Outline each Plasmodium vivax-infected red blood cell.
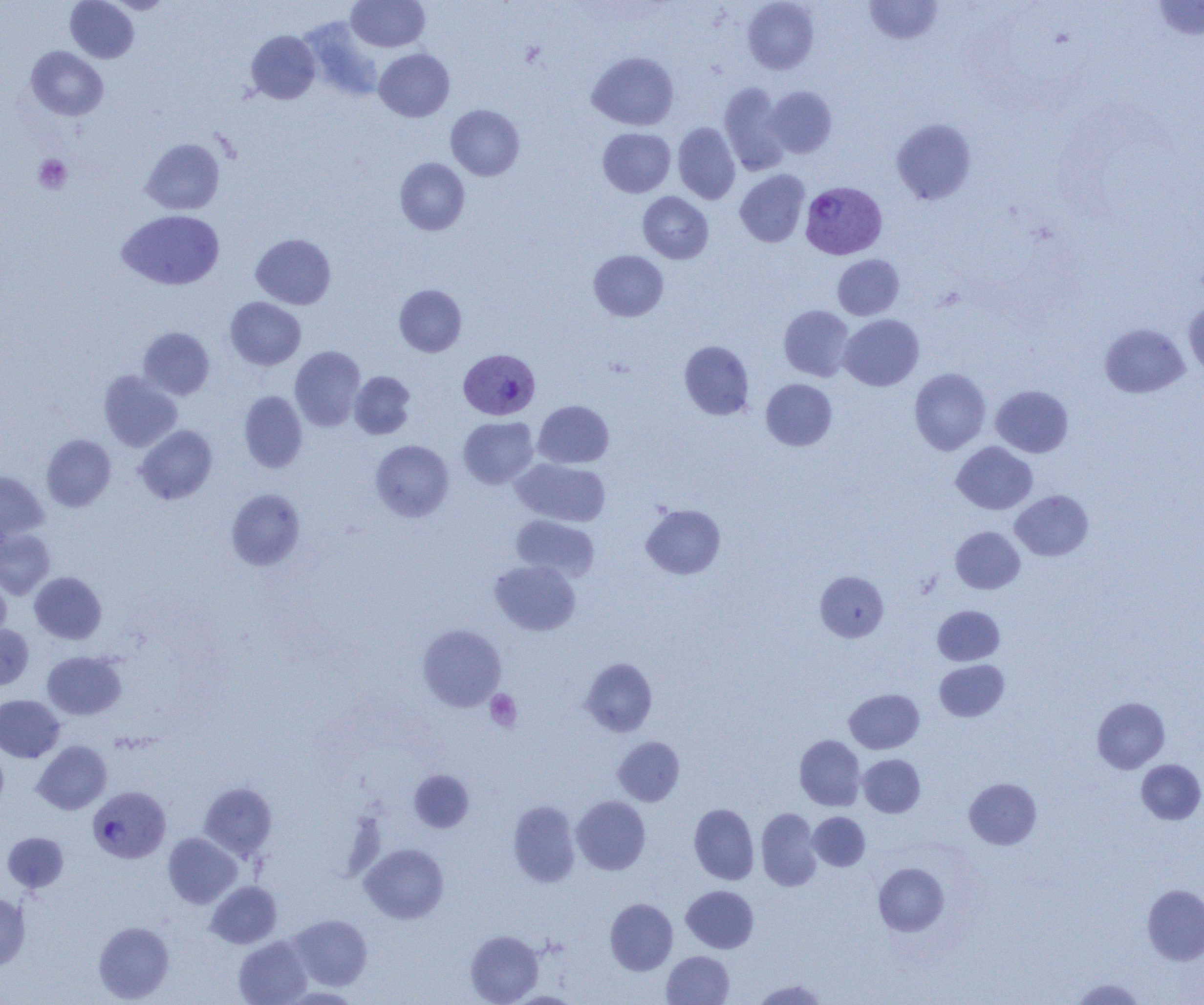
Approximate bounding boxes as named x1/y1/x2/y2 corners in pixels.
Plasmodium vivax-infected red blood cells: (x1=800, y1=181, x2=887, y2=259), (x1=459, y1=348, x2=541, y2=420), (x1=88, y1=786, x2=170, y2=863).

Uninfected red blood cell locations: (x1=65, y1=0, x2=138, y2=63), (x1=106, y1=0, x2=174, y2=14), (x1=347, y1=0, x2=430, y2=52), (x1=864, y1=0, x2=944, y2=45), (x1=1151, y1=0, x2=1204, y2=42), (x1=742, y1=1, x2=819, y2=74), (x1=300, y1=17, x2=383, y2=102), (x1=246, y1=31, x2=320, y2=104), (x1=26, y1=46, x2=108, y2=121), (x1=374, y1=48, x2=454, y2=121), (x1=587, y1=51, x2=679, y2=130), (x1=719, y1=83, x2=790, y2=175), (x1=765, y1=86, x2=837, y2=157), (x1=446, y1=104, x2=525, y2=180), (x1=891, y1=118, x2=976, y2=205), (x1=673, y1=122, x2=741, y2=204), (x1=597, y1=127, x2=675, y2=198), (x1=141, y1=138, x2=225, y2=215), (x1=395, y1=157, x2=469, y2=235), (x1=735, y1=169, x2=810, y2=247), (x1=638, y1=192, x2=713, y2=264), (x1=117, y1=209, x2=224, y2=290), (x1=251, y1=233, x2=336, y2=309), (x1=588, y1=250, x2=668, y2=322), (x1=832, y1=254, x2=904, y2=320), (x1=394, y1=285, x2=466, y2=356), (x1=225, y1=297, x2=306, y2=370), (x1=1184, y1=298, x2=1204, y2=378), (x1=778, y1=305, x2=854, y2=381), (x1=838, y1=314, x2=924, y2=391), (x1=1100, y1=323, x2=1189, y2=398), (x1=138, y1=327, x2=214, y2=399), (x1=679, y1=340, x2=754, y2=420), (x1=290, y1=346, x2=366, y2=430), (x1=909, y1=367, x2=991, y2=455), (x1=99, y1=371, x2=182, y2=452), (x1=349, y1=371, x2=416, y2=439), (x1=761, y1=379, x2=837, y2=451), (x1=991, y1=385, x2=1073, y2=458), (x1=239, y1=391, x2=308, y2=473), (x1=533, y1=400, x2=614, y2=468), (x1=458, y1=416, x2=538, y2=488), (x1=135, y1=425, x2=217, y2=504), (x1=41, y1=434, x2=116, y2=511), (x1=370, y1=440, x2=454, y2=521), (x1=951, y1=441, x2=1037, y2=514), (x1=511, y1=458, x2=610, y2=526), (x1=0, y1=470, x2=48, y2=544), (x1=226, y1=489, x2=305, y2=570), (x1=1010, y1=490, x2=1094, y2=561), (x1=641, y1=504, x2=725, y2=579), (x1=511, y1=515, x2=599, y2=581), (x1=950, y1=526, x2=1025, y2=593), (x1=0, y1=529, x2=55, y2=600), (x1=490, y1=560, x2=580, y2=635), (x1=815, y1=571, x2=888, y2=642), (x1=30, y1=572, x2=107, y2=644), (x1=0, y1=573, x2=11, y2=643), (x1=933, y1=605, x2=1004, y2=665), (x1=0, y1=624, x2=33, y2=690), (x1=417, y1=624, x2=506, y2=712), (x1=42, y1=651, x2=126, y2=719), (x1=580, y1=658, x2=657, y2=736), (x1=934, y1=660, x2=1009, y2=722), (x1=844, y1=689, x2=924, y2=753), (x1=0, y1=695, x2=65, y2=762), (x1=1092, y1=697, x2=1170, y2=774), (x1=794, y1=735, x2=865, y2=810), (x1=612, y1=736, x2=685, y2=806), (x1=33, y1=741, x2=111, y2=814), (x1=0, y1=745, x2=9, y2=815), (x1=858, y1=754, x2=925, y2=817), (x1=1136, y1=759, x2=1204, y2=824), (x1=410, y1=770, x2=474, y2=831), (x1=964, y1=777, x2=1042, y2=849), (x1=198, y1=782, x2=276, y2=860), (x1=571, y1=796, x2=651, y2=874), (x1=508, y1=801, x2=580, y2=887), (x1=689, y1=804, x2=759, y2=885), (x1=756, y1=807, x2=822, y2=891), (x1=808, y1=812, x2=870, y2=871), (x1=2, y1=832, x2=69, y2=892), (x1=163, y1=833, x2=242, y2=908), (x1=360, y1=843, x2=449, y2=924), (x1=873, y1=862, x2=949, y2=936), (x1=206, y1=881, x2=281, y2=948), (x1=1142, y1=884, x2=1204, y2=965), (x1=681, y1=885, x2=759, y2=953), (x1=0, y1=892, x2=30, y2=971), (x1=605, y1=898, x2=678, y2=975), (x1=288, y1=915, x2=372, y2=991), (x1=93, y1=921, x2=174, y2=1002), (x1=465, y1=930, x2=543, y2=1004), (x1=234, y1=935, x2=312, y2=1005), (x1=662, y1=951, x2=734, y2=1004), (x1=1071, y1=978, x2=1144, y2=1004), (x1=751, y1=979, x2=827, y2=1004). Platelet locations: (x1=34, y1=154, x2=72, y2=193), (x1=485, y1=690, x2=522, y2=731). Slide-level diagnosis: Plasmodium vivax. 1000x magnification. Optical microscopy. Image is 1204×1005 pixels. Single field of view. Thin blood smear.